Report the malaria status of this cell.
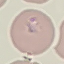
It is parasitized.

Summary:
  - Stain: Giemsa
  - Preparation: thin smear
  - Capture: smartphone camera at the microscope eyepiece
  - Image type: automatically extracted cell patch, resized to 64 × 64 pixels